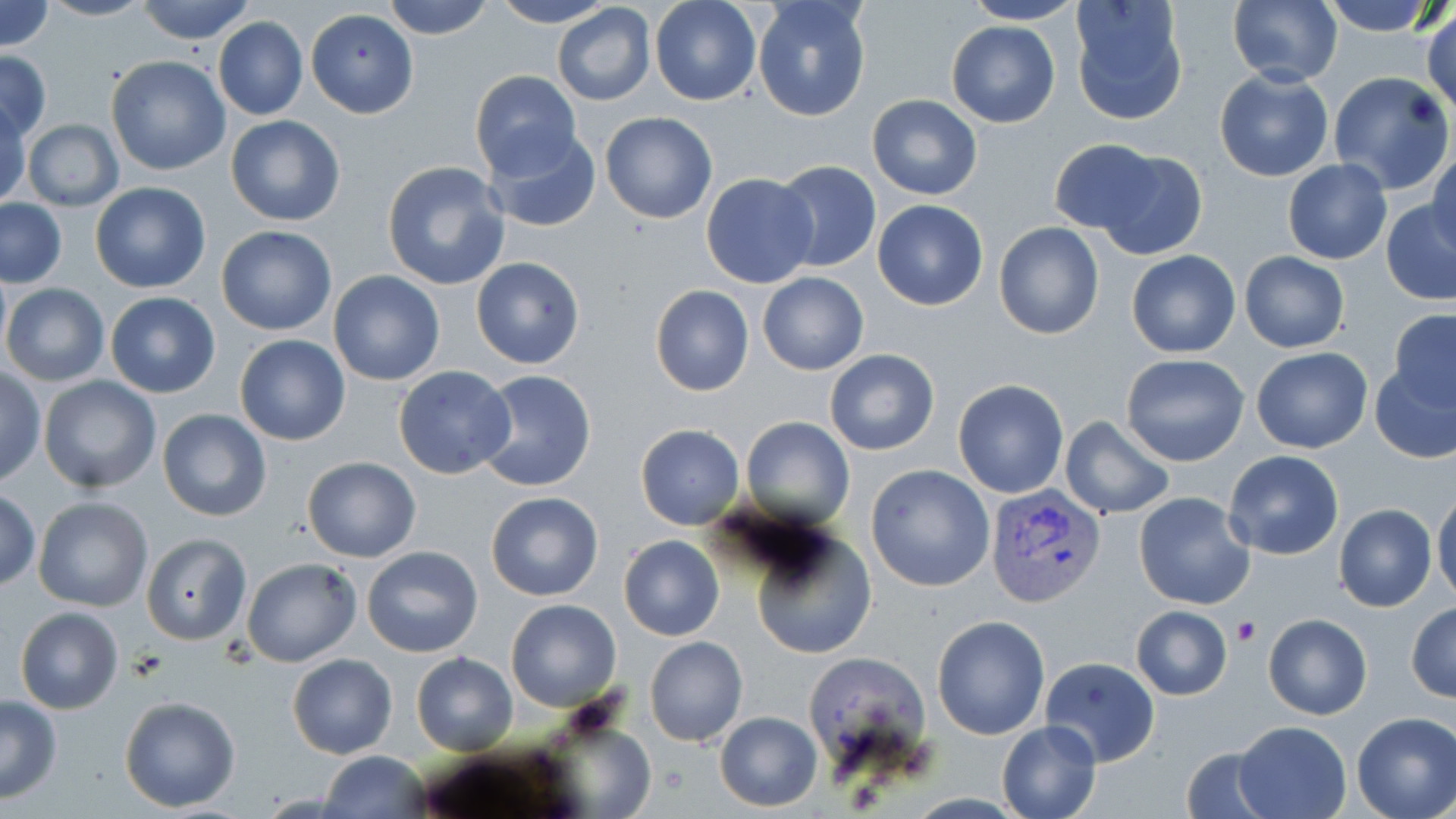
slide-level diagnosis = Plasmodium vivax
platelet locations = approximate bounding boxes as (x1, y1, x2, y2) in pixels: (1232, 617, 1261, 645)
field of view = one of a larger specimen
modality = optical microscopy
stain = May-Grünwald-Giemsa
uninfected red blood cell locations = approximate bounding boxes as (x1, y1, x2, y2) in pixels: (0, 0, 54, 53), (38, 0, 153, 22), (135, 0, 256, 44), (382, 0, 494, 41), (490, 0, 618, 27), (650, 0, 761, 106), (1068, 0, 1190, 127), (1227, 0, 1344, 88), (1315, 0, 1447, 36), (961, 1, 1086, 24), (751, 2, 871, 122), (551, 4, 656, 106), (1423, 8, 1455, 119), (305, 9, 418, 119), (213, 17, 307, 120), (946, 21, 1062, 128), (0, 50, 51, 142), (106, 56, 231, 176), (1214, 68, 1335, 182), (471, 70, 580, 178), (1326, 73, 1453, 195), (865, 94, 981, 200), (1, 98, 29, 210), (600, 112, 718, 224), (225, 115, 346, 226), (22, 118, 124, 213), (483, 124, 600, 234), (1047, 138, 1167, 237), (1427, 147, 1456, 257), (1093, 148, 1207, 259), (382, 159, 510, 292), (1282, 159, 1394, 264), (772, 160, 882, 274), (701, 172, 820, 289), (89, 182, 212, 294), (1, 198, 67, 288), (872, 200, 989, 311), (1382, 201, 1456, 304), (994, 222, 1105, 339), (216, 225, 337, 337), (1127, 249, 1240, 358), (1239, 250, 1349, 352), (471, 256, 586, 370), (328, 270, 446, 386), (758, 272, 869, 375), (2, 284, 109, 386), (650, 284, 754, 396), (105, 292, 222, 398), (1388, 309, 1456, 411), (233, 333, 350, 446), (1251, 346, 1373, 454), (824, 348, 940, 455), (1119, 353, 1251, 466), (1369, 363, 1456, 462), (392, 366, 517, 480), (0, 368, 45, 485), (475, 370, 598, 493), (38, 376, 160, 494), (952, 379, 1069, 498), (156, 408, 272, 522), (740, 416, 854, 529), (1060, 416, 1175, 519), (635, 425, 744, 530), (1223, 450, 1345, 559), (301, 456, 421, 562), (867, 463, 995, 592), (1431, 488, 1456, 604), (0, 489, 41, 591), (1133, 490, 1254, 610), (485, 492, 604, 602), (33, 496, 153, 611), (1334, 504, 1437, 613), (752, 530, 878, 662), (142, 535, 251, 644), (619, 536, 724, 641), (362, 546, 483, 658), (242, 557, 361, 667), (505, 599, 623, 712), (1406, 603, 1456, 703), (1130, 605, 1232, 701), (14, 606, 124, 714), (1262, 613, 1372, 720), (932, 615, 1050, 739), (644, 636, 747, 747), (286, 653, 397, 759), (411, 653, 518, 755), (1040, 656, 1161, 767), (0, 694, 63, 803), (118, 695, 241, 813), (715, 711, 822, 812), (1351, 712, 1456, 819), (996, 719, 1103, 819), (1233, 721, 1350, 819), (1177, 743, 1278, 818), (320, 751, 429, 818)
image size = 1456×819 pixels
Plasmodium vivax-infected red blood cell locations = approximate bounding boxes as (x1, y1, x2, y2) in pixels: (986, 483, 1106, 606)
preparation = thin blood smear
magnification = 1000x